Classify this cell by malaria status.
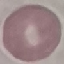

It is uninfected.

Summary:
  - Image type: automatically extracted cell patch, resized to 64 × 64 pixels
  - Stain: Giemsa
  - Preparation: thin blood smear
  - Capture: smartphone through the microscope eyepiece